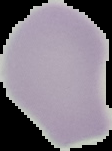
Result: negative for Plasmodium parasites. Segmented cell region on a black background. From a thin blood film. Image is 112×151 pixels.